Classify this cell by malaria status.
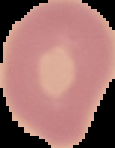
Uninfected.

image_size: 115×148 pixels
preparation: thin blood smear
image_type: segmented cell region on a black background